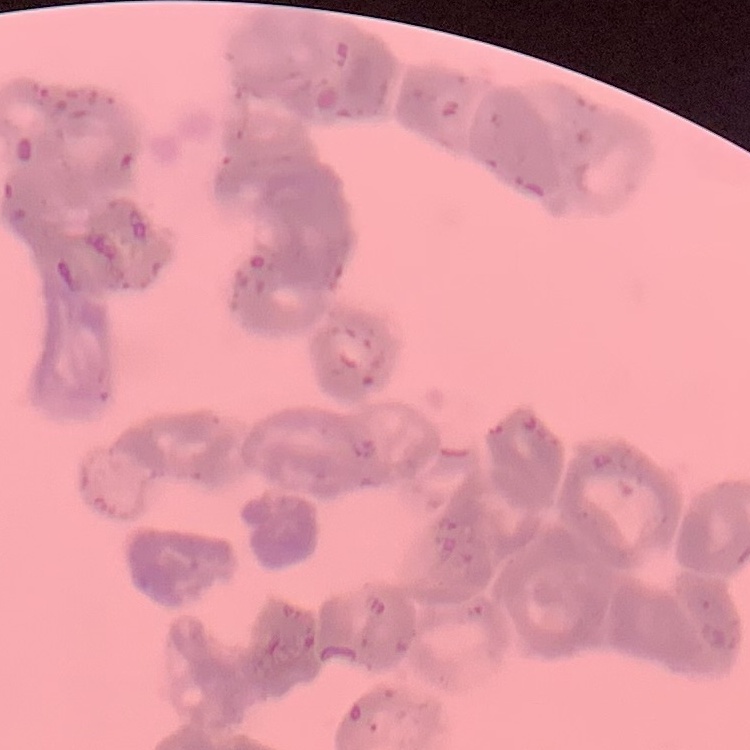

red blood cell morphology = rouleaux formation
preparation = thin blood smear
image type = one tile cut from a larger photomicrograph
stain = Field's or Giemsa